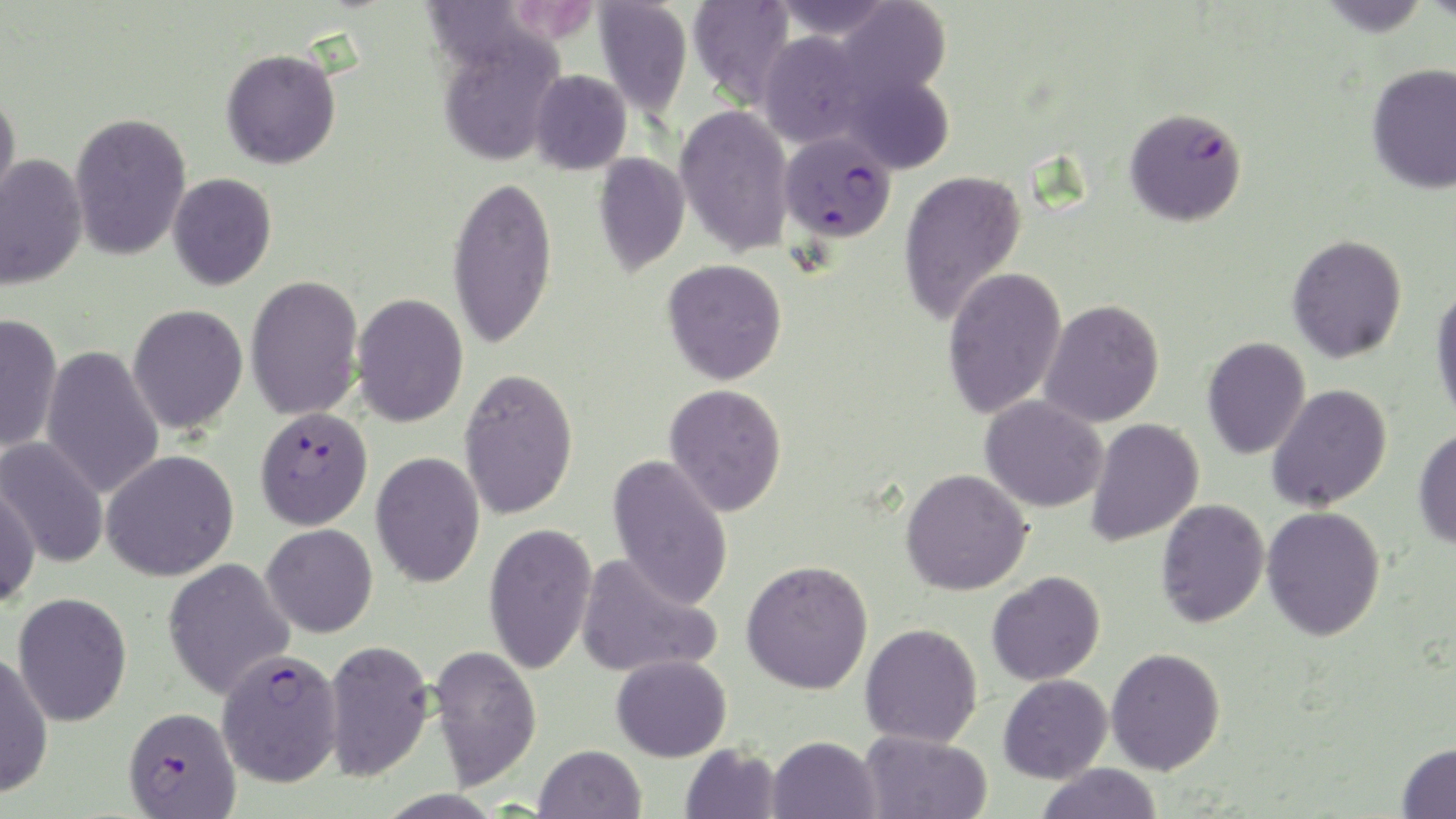

slide-level diagnosis = Plasmodium falciparum
image size = 1456×819 pixels
platelet locations = approximate bounding boxes as (x1, y1, x2, y2) in pixels: (507, 2, 601, 42)
uninfected red blood cell locations = approximate bounding boxes as (x1, y1, x2, y2) in pixels: (594, 0, 692, 118), (688, 0, 796, 107), (772, 0, 896, 40), (1315, 0, 1432, 36), (836, 1, 952, 101), (436, 28, 565, 166), (758, 30, 872, 148), (221, 49, 341, 169), (1367, 63, 1456, 194), (529, 70, 632, 175), (840, 72, 955, 175), (0, 90, 21, 214), (675, 105, 794, 257), (69, 112, 191, 262), (592, 151, 690, 276), (0, 153, 87, 291), (898, 169, 1027, 327), (168, 173, 277, 291), (447, 174, 557, 350), (1287, 234, 1408, 363), (662, 258, 787, 385), (942, 265, 1067, 419), (245, 274, 364, 421), (1430, 283, 1456, 428), (351, 293, 468, 427), (1039, 299, 1165, 427), (127, 304, 248, 434), (0, 313, 63, 453), (1202, 336, 1310, 459), (41, 345, 164, 500), (459, 367, 579, 520), (664, 383, 788, 517), (1267, 384, 1393, 512), (980, 394, 1108, 512), (1085, 417, 1204, 547), (1413, 427, 1456, 550), (1, 437, 109, 570), (101, 449, 240, 581), (371, 451, 485, 588), (606, 454, 734, 611), (901, 468, 1033, 596), (0, 482, 41, 609), (1156, 498, 1270, 628), (1261, 506, 1386, 641), (483, 521, 597, 675), (261, 524, 378, 637), (576, 552, 722, 679), (162, 557, 295, 700), (741, 559, 874, 695), (987, 571, 1105, 685), (13, 592, 133, 727), (860, 623, 983, 747), (323, 638, 434, 782), (427, 644, 542, 790), (1106, 647, 1225, 775), (0, 653, 54, 799), (611, 654, 732, 762), (998, 674, 1112, 784), (859, 730, 992, 819), (766, 735, 882, 819), (1397, 742, 1456, 818), (680, 743, 781, 819), (534, 744, 646, 819), (1035, 763, 1163, 818)
stain = May-Grünwald-Giemsa
field of view = one of a larger specimen
modality = optical microscopy
preparation = thin blood film
magnification = 1000x
Plasmodium falciparum-infected red blood cell locations = approximate bounding boxes as (x1, y1, x2, y2) in pixels: (1124, 107, 1247, 226), (779, 130, 896, 243), (255, 406, 373, 530), (216, 648, 344, 788), (123, 705, 242, 819)